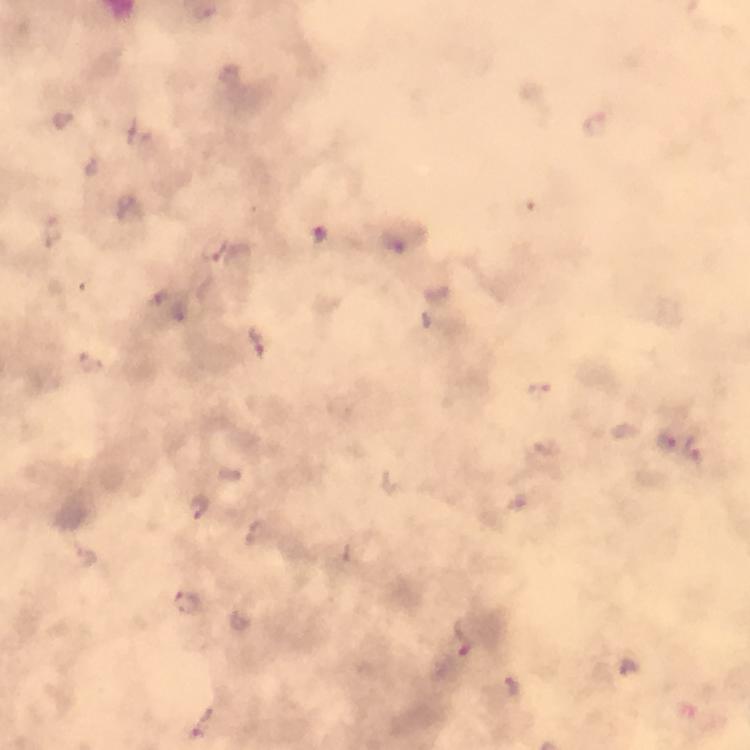

Approximate centers as (x, y) in pixels.
Summary:
  - Plasmodium parasite locations: (596, 124), (320, 231), (396, 245), (258, 345), (540, 387), (668, 439), (694, 447), (198, 509), (187, 602), (464, 638), (513, 686), (201, 723)
  - Preparation: thick blood film
  - Magnification: 100x
  - Immersion oil: applied
  - Context: from a malaria diagnostic workup
  - Capture: smartphone mounted on the microscope
  - Cropped from: a single field of view
  - Stain: Giemsa
  - Image size: 750×750 pixels